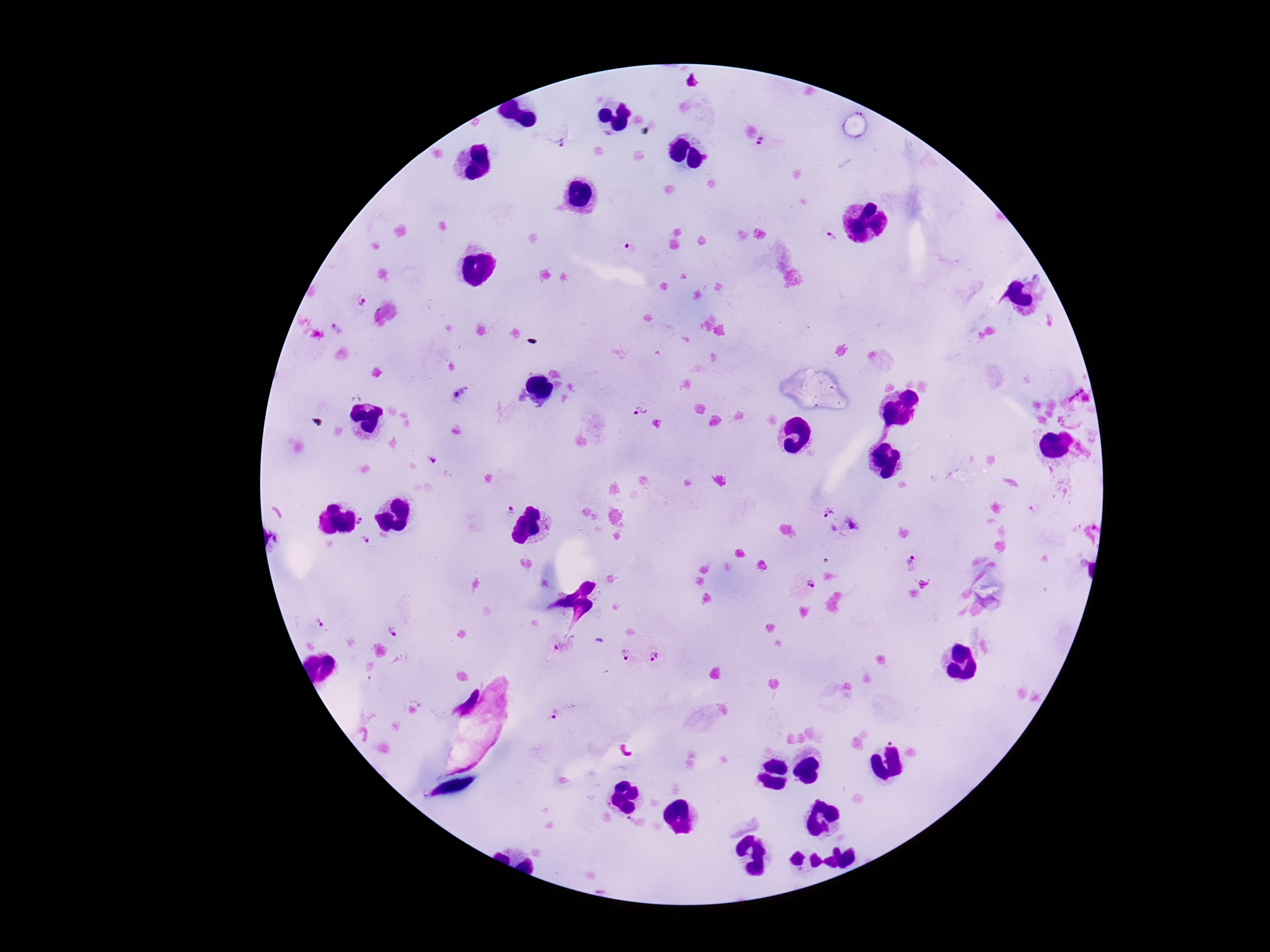
Approximate centers as [x, y] in pixels. Plasmodium parasite locations: [558, 141], [766, 144], [827, 239], [627, 246], [359, 300], [336, 328], [640, 411], [431, 458], [509, 511], [827, 513], [363, 521], [851, 525], [366, 539], [912, 562], [806, 583], [318, 622], [392, 632], [562, 649], [626, 656], [656, 657], [555, 714]. Thick peripheral-blood smear. Giemsa-stained preparation. Image is 1270×952 pixels. One field from this slide. Patient malaria status: positive. 100x magnification. Smartphone photograph taken through the microscope eyepiece.